Assess this cell for malaria.
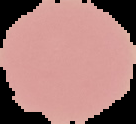
It is uninfected.

Cell region segmented out of the field of view; the surrounding area is masked to black. Image is 136×124 pixels. From a thin blood film.